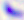

Summary:
  - Modality: micrograph
  - Magnification: 400x
  - Identification: Toxoplasma gondii